Give the preparation type.
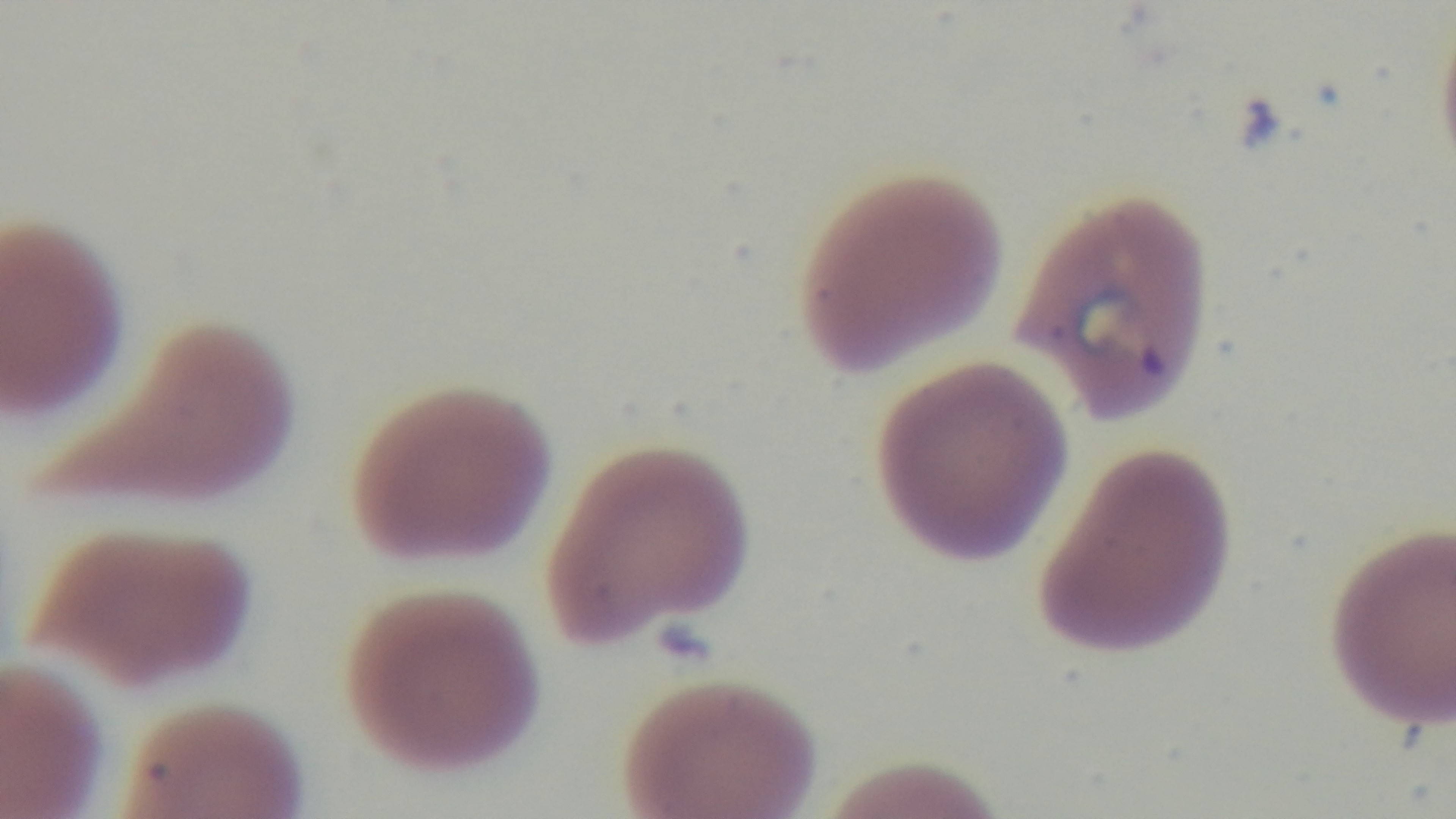

A thin smear.

malaria status = positive
capture = mounted 4K digital camera
field of view = one from the slide
modality = light microscopy
objective = 100x oil immersion
stain = Giemsa